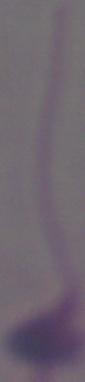
modality = micrograph
magnification = 1000x
identification = Leishmania